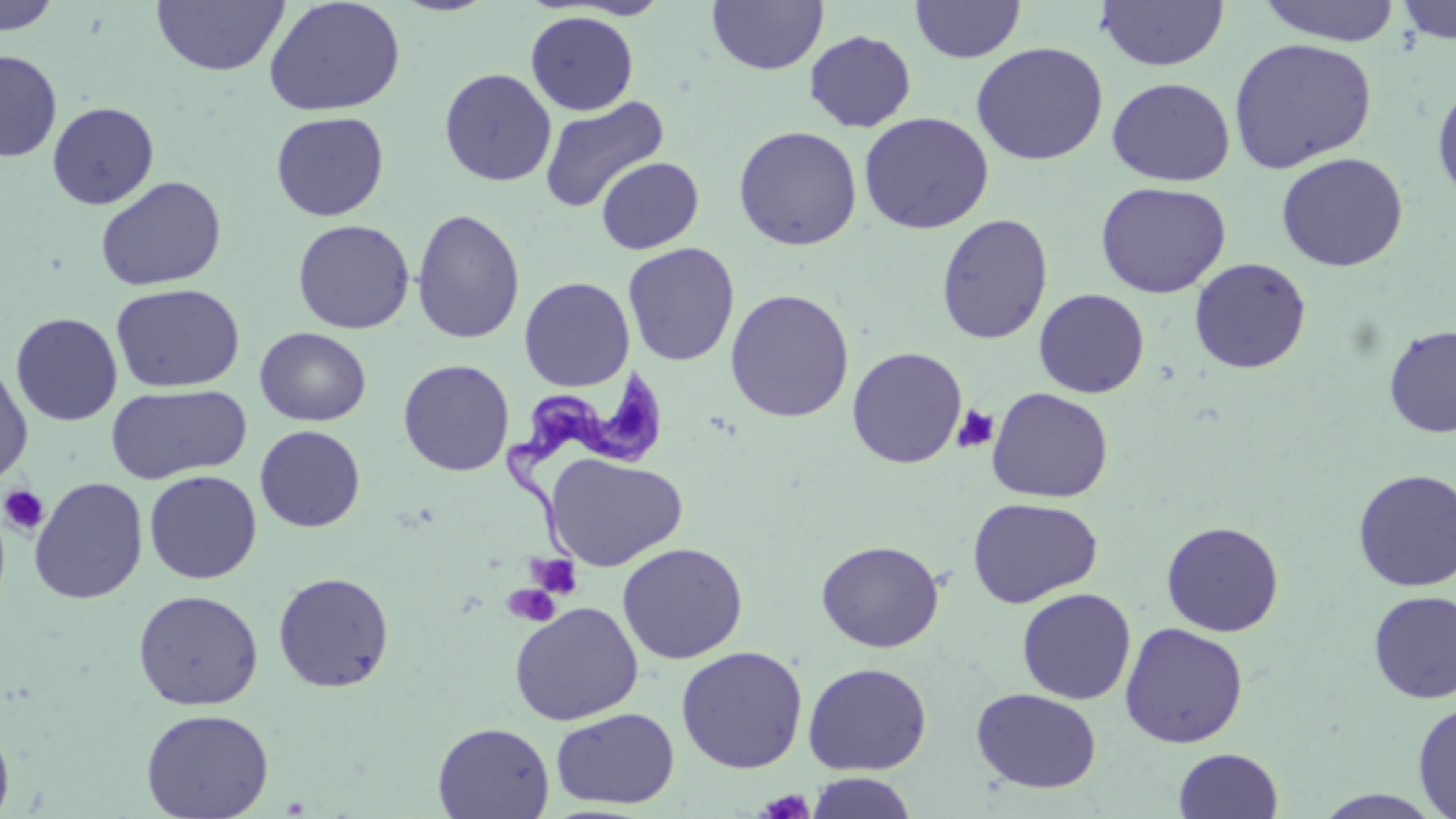

slide-level diagnosis = Trypanosoma brucei
image size = 1456×819 pixels
platelet locations = approximate bounding boxes as named x1/y1/x2/y2 corners in pixels: (x1=951, y1=405, x2=999, y2=454), (x1=1, y1=484, x2=50, y2=536), (x1=526, y1=553, x2=584, y2=600), (x1=502, y1=584, x2=561, y2=628), (x1=757, y1=788, x2=815, y2=818)
magnification = 1000x
Trypanosoma brucei locations = approximate bounding boxes as named x1/y1/x2/y2 corners in pixels: (x1=503, y1=362, x2=670, y2=564)
modality = light microscopy
uninfected red blood cell locations = approximate bounding boxes as named x1/y1/x2/y2 corners in pixels: (x1=0, y1=0, x2=62, y2=36), (x1=151, y1=0, x2=289, y2=77), (x1=707, y1=0, x2=828, y2=76), (x1=911, y1=0, x2=1026, y2=63), (x1=1094, y1=0, x2=1228, y2=71), (x1=1257, y1=0, x2=1403, y2=46), (x1=1395, y1=0, x2=1456, y2=45), (x1=263, y1=1, x2=406, y2=117), (x1=561, y1=1, x2=673, y2=20), (x1=525, y1=11, x2=639, y2=116), (x1=804, y1=30, x2=917, y2=132), (x1=1227, y1=37, x2=1378, y2=173), (x1=970, y1=42, x2=1108, y2=165), (x1=0, y1=49, x2=62, y2=163), (x1=439, y1=68, x2=557, y2=187), (x1=1432, y1=76, x2=1456, y2=208), (x1=1107, y1=77, x2=1235, y2=186), (x1=540, y1=96, x2=669, y2=214), (x1=47, y1=101, x2=159, y2=210), (x1=270, y1=111, x2=389, y2=221), (x1=858, y1=112, x2=994, y2=234), (x1=732, y1=126, x2=863, y2=250), (x1=1275, y1=151, x2=1409, y2=272), (x1=595, y1=156, x2=704, y2=254), (x1=95, y1=175, x2=226, y2=291), (x1=1095, y1=181, x2=1231, y2=298), (x1=411, y1=208, x2=525, y2=345), (x1=936, y1=214, x2=1053, y2=345), (x1=292, y1=219, x2=415, y2=335), (x1=622, y1=242, x2=740, y2=366), (x1=1189, y1=257, x2=1311, y2=374), (x1=519, y1=277, x2=635, y2=392), (x1=110, y1=283, x2=245, y2=393), (x1=725, y1=288, x2=855, y2=423), (x1=1033, y1=289, x2=1150, y2=398), (x1=10, y1=312, x2=123, y2=426), (x1=1383, y1=325, x2=1456, y2=438), (x1=254, y1=327, x2=372, y2=427), (x1=846, y1=347, x2=967, y2=469), (x1=0, y1=357, x2=33, y2=488), (x1=398, y1=358, x2=515, y2=477), (x1=106, y1=383, x2=251, y2=483), (x1=987, y1=387, x2=1114, y2=503), (x1=254, y1=425, x2=365, y2=532), (x1=546, y1=453, x2=687, y2=571), (x1=144, y1=469, x2=262, y2=584), (x1=1353, y1=469, x2=1456, y2=592), (x1=28, y1=476, x2=148, y2=604), (x1=967, y1=497, x2=1103, y2=608), (x1=1161, y1=520, x2=1285, y2=637), (x1=815, y1=539, x2=945, y2=652), (x1=616, y1=542, x2=748, y2=664), (x1=272, y1=571, x2=395, y2=693), (x1=1017, y1=588, x2=1136, y2=705), (x1=132, y1=589, x2=264, y2=710), (x1=1368, y1=590, x2=1456, y2=703), (x1=509, y1=601, x2=644, y2=726), (x1=1120, y1=622, x2=1248, y2=748), (x1=675, y1=645, x2=808, y2=774), (x1=802, y1=662, x2=933, y2=776), (x1=971, y1=688, x2=1102, y2=793), (x1=1413, y1=701, x2=1456, y2=818), (x1=550, y1=707, x2=680, y2=809), (x1=140, y1=708, x2=274, y2=819), (x1=0, y1=718, x2=15, y2=819), (x1=432, y1=721, x2=555, y2=818), (x1=1173, y1=747, x2=1284, y2=819), (x1=805, y1=772, x2=919, y2=819), (x1=1312, y1=789, x2=1447, y2=818)
stain = May-Grünwald-Giemsa
field of view = single
preparation = thin blood smear